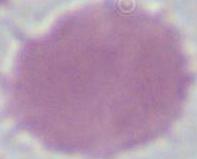

magnification = 1000x
identification = erythrocyte
modality = micrograph